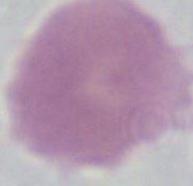

Summary:
  - Identification: red blood cell
  - Magnification: 1000x
  - Modality: photomicrograph